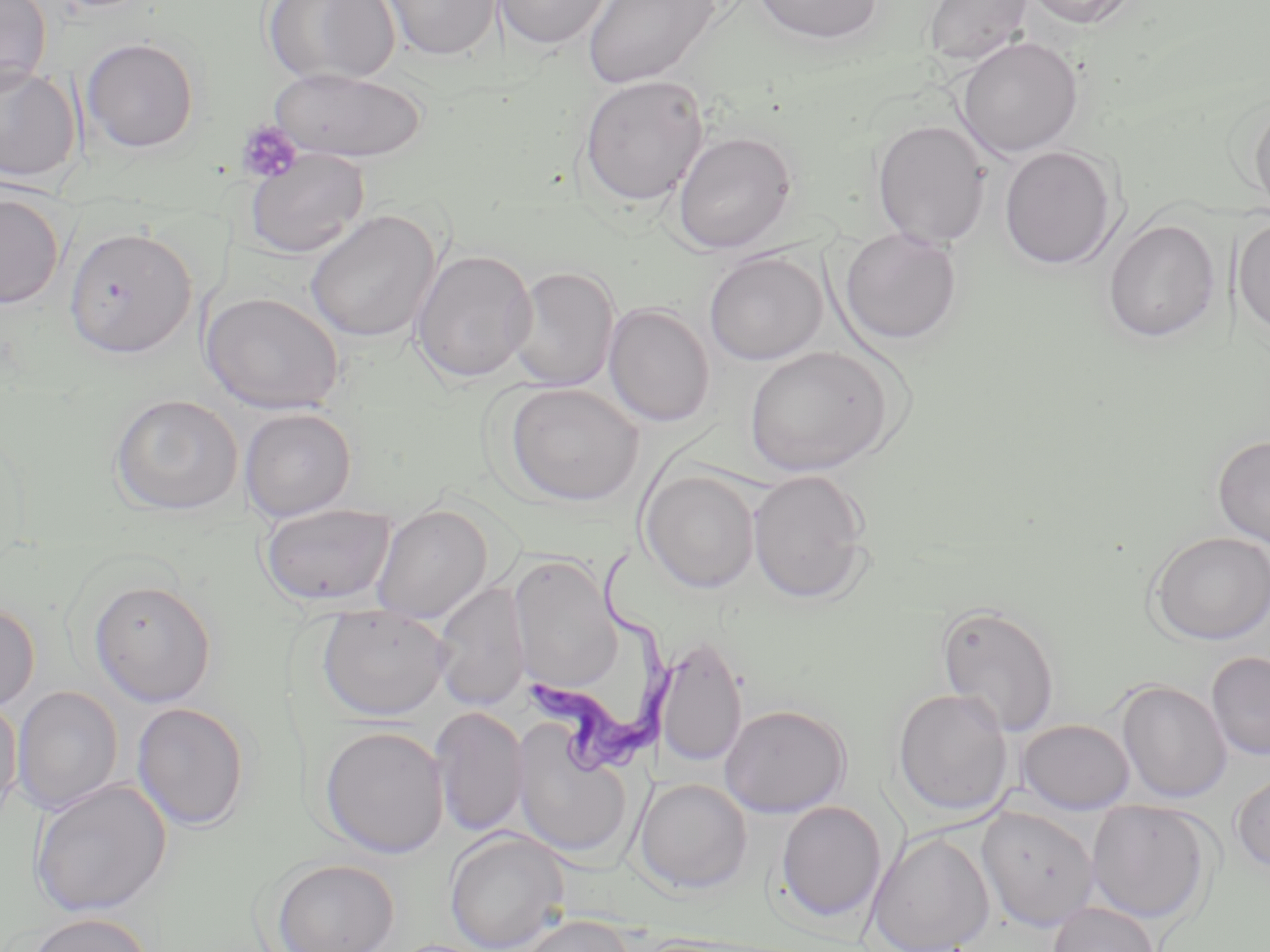

slide-level diagnosis = Trypanosoma brucei
stain = May-Grünwald-Giemsa
preparation = thin blood film
platelet locations = approximate bounding boxes as [x1, y1, x2, y2] in pixels: [235, 120, 303, 184]
field of view = single
magnification = 1000x
modality = optical microscopy
uninfected red blood cell locations = approximate bounding boxes as [x1, y1, x2, y2] in pixels: [0, 0, 52, 96], [263, 0, 399, 85], [380, 0, 503, 62], [493, 0, 614, 50], [582, 0, 720, 89], [752, 0, 886, 45], [922, 0, 1033, 65], [1022, 0, 1141, 29], [954, 36, 1084, 159], [81, 37, 200, 153], [0, 63, 82, 183], [268, 67, 427, 162], [577, 74, 709, 208], [1247, 99, 1270, 214], [871, 119, 991, 248], [671, 130, 798, 253], [999, 145, 1119, 270], [244, 149, 370, 258], [0, 192, 66, 309], [304, 210, 440, 343], [1232, 215, 1270, 338], [1102, 218, 1220, 343], [64, 226, 196, 359], [839, 226, 963, 346], [411, 249, 538, 384], [704, 250, 828, 366], [506, 266, 621, 392], [202, 291, 345, 415], [603, 303, 715, 428], [743, 346, 894, 476], [504, 383, 645, 506], [109, 393, 244, 516], [239, 408, 357, 522], [1212, 434, 1270, 546], [640, 469, 760, 593], [747, 469, 872, 604], [259, 503, 397, 608], [370, 504, 493, 625], [1148, 531, 1270, 645], [508, 554, 622, 692], [88, 578, 217, 707], [432, 580, 531, 712], [0, 602, 39, 713], [935, 602, 1061, 737], [316, 604, 453, 721], [654, 634, 748, 769], [1205, 650, 1270, 761], [1116, 679, 1232, 804], [11, 686, 124, 813], [892, 687, 1013, 817], [0, 695, 23, 823], [131, 702, 250, 830], [719, 703, 851, 817], [431, 706, 530, 837], [1016, 718, 1135, 814], [510, 721, 635, 862], [319, 726, 449, 859], [1230, 771, 1270, 875], [633, 777, 753, 894], [28, 778, 172, 917], [1085, 799, 1215, 925], [773, 800, 887, 924], [976, 806, 1100, 931], [443, 829, 570, 952], [866, 831, 995, 952], [270, 858, 400, 952], [1048, 901, 1160, 952], [23, 912, 153, 952], [510, 914, 636, 952]
Trypanosoma brucei locations = approximate bounding boxes as [x1, y1, x2, y2] in pixels: [527, 543, 683, 778]
image size = 1270×952 pixels